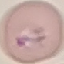
Summary:
  - Result: malaria parasites detected
  - Capture: smartphone through the microscope eyepiece
  - Stain: Giemsa
  - Preparation: thin blood film
  - Image type: cell patch, automatically extracted from a larger field of view and resized to 64 × 64 pixels